Identify the parasite.
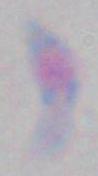

Toxoplasma gondii.

Photomicrograph. Captured at 1000x magnification.